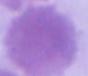
Photomicrograph. 1000x magnification. An erythrocyte is shown.